Give the extent of all Plasmodium falciparum-infected red blood cells.
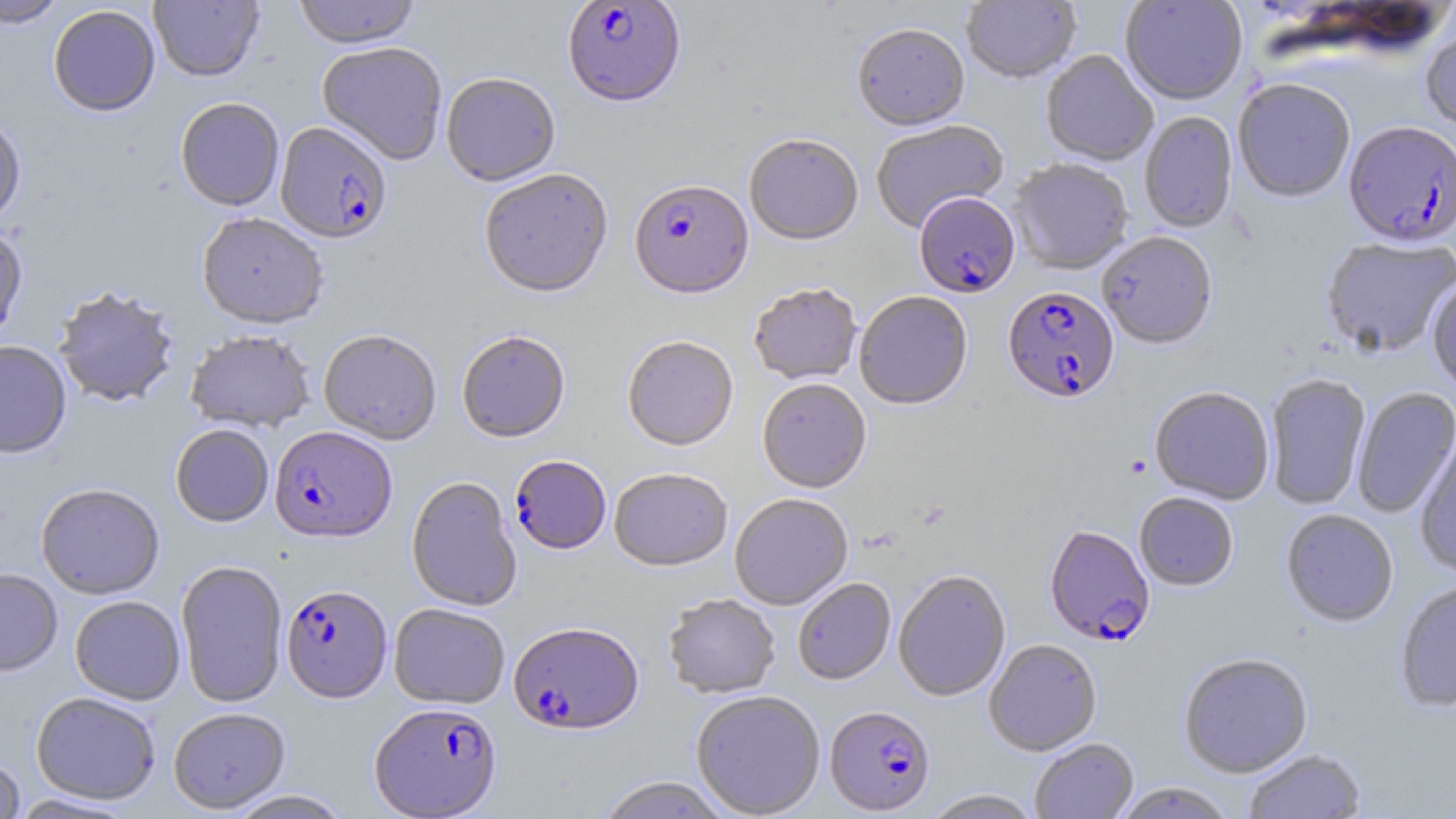

Approximate bounding boxes as (x1,y1)-(x2,y2) corner pairs in pixels.
Plasmodium falciparum-infected red blood cells: (562,1)-(686,111), (275,124)-(392,247), (1343,124)-(1455,251), (628,181)-(754,302), (914,194)-(1020,300), (1003,288)-(1120,406), (269,427)-(397,546), (510,456)-(611,557), (1044,527)-(1155,649), (281,586)-(393,705), (508,624)-(644,737), (369,704)-(502,818), (825,706)-(936,816).

Summary:
  - Uninfected red blood cell locations: (1,0)-(68,29), (149,0)-(264,84), (292,0)-(422,52), (1120,0)-(1248,107), (961,1)-(1082,86), (48,5)-(161,118), (852,26)-(970,134), (1421,27)-(1456,138), (317,44)-(448,166), (1040,51)-(1158,168), (441,74)-(561,189), (1233,81)-(1355,205), (175,99)-(285,213), (1138,112)-(1238,234), (0,119)-(26,229), (871,121)-(1010,233), (744,136)-(863,248), (1008,161)-(1134,277), (479,171)-(614,302), (196,215)-(328,332), (0,227)-(28,348), (1097,234)-(1217,352), (1320,238)-(1456,359), (1427,277)-(1456,395), (749,285)-(862,387), (53,287)-(179,409), (855,292)-(973,412), (319,331)-(441,446), (185,332)-(315,435), (457,333)-(571,445), (622,337)-(738,453), (0,342)-(72,461), (1264,374)-(1371,511), (757,380)-(871,495), (1352,386)-(1456,518), (1149,388)-(1274,506), (171,426)-(274,528), (1415,440)-(1456,575), (610,470)-(733,574), (407,478)-(521,612), (36,486)-(165,601), (1134,493)-(1238,592), (730,495)-(853,611), (1281,510)-(1398,628), (175,561)-(289,708), (0,570)-(63,678), (894,571)-(1011,703), (793,579)-(896,686), (1395,581)-(1456,713), (663,595)-(780,700), (70,597)-(185,706), (389,604)-(510,710), (984,640)-(1102,757), (1178,653)-(1313,779), (690,691)-(826,818), (31,693)-(161,805), (168,709)-(291,815), (1030,738)-(1139,819), (1243,749)-(1367,819), (0,757)-(25,819), (596,776)-(733,819), (1113,782)-(1236,818), (225,789)-(353,818), (922,789)-(1043,818), (8,794)-(140,818)
  - Slide-level diagnosis: Plasmodium falciparum
  - Preparation: thin blood smear
  - Modality: light microscopy
  - Field of view: one of a larger specimen
  - Image size: 1456×819 pixels
  - Stain: May-Grünwald-Giemsa
  - Magnification: 1000x